Comment on the morphology of the erythrocytes.
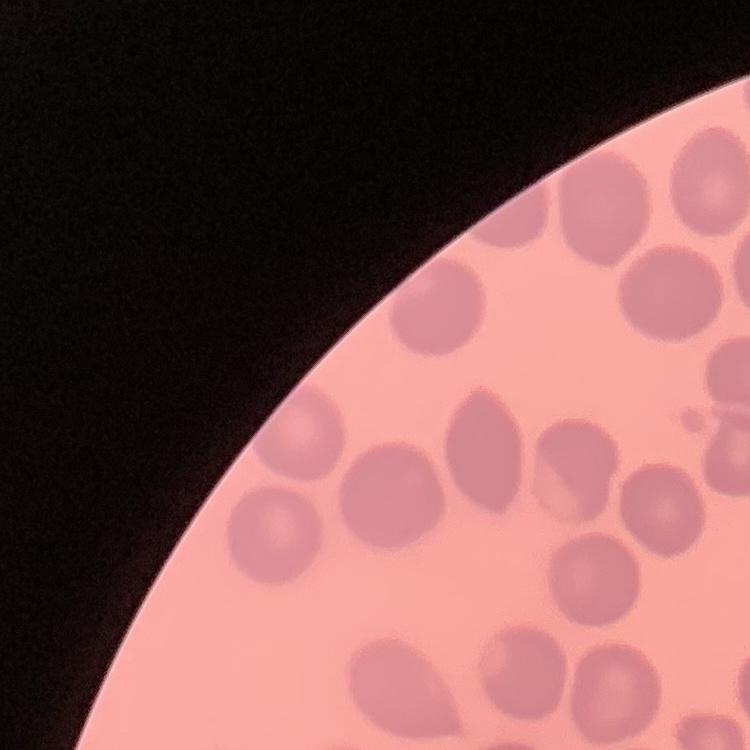
No rouleaux formation.

Thin blood smear. Square crop of a larger photomicrograph. Stained with either Field's or Giemsa.